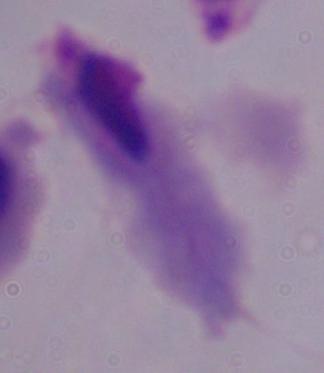
Summary:
  - Modality: photomicrograph
  - Identification: trichomonad
  - Magnification: 1000x